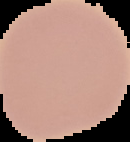
image size = 130×142 pixels
preparation = thin blood smear
image type = segmented cell region with the area outside set to black
result = negative for Plasmodium parasites